Describe the morphology of the erythrocytes.
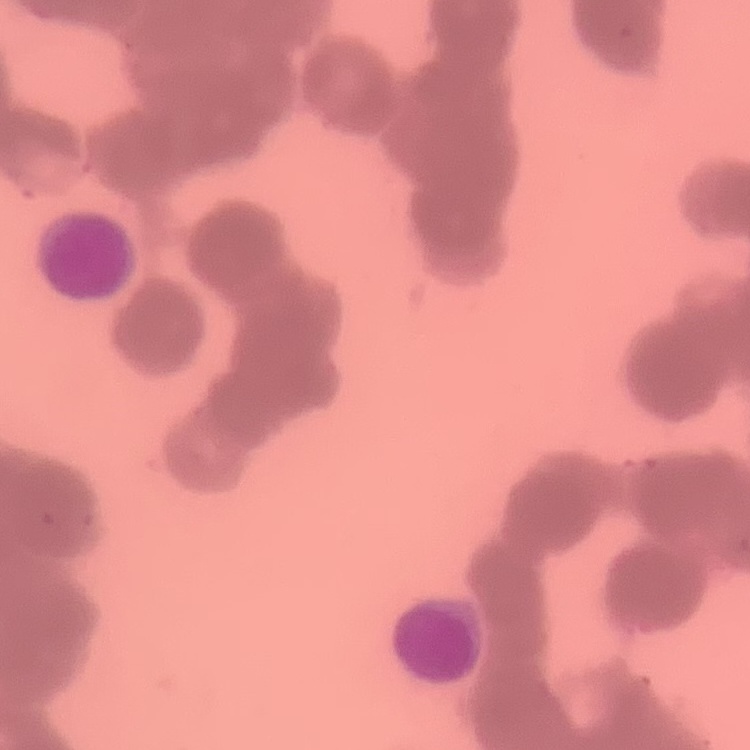

They show rouleaux formation.

Field's or Giemsa stain. Thin blood smear. Square crop of a larger photomicrograph.